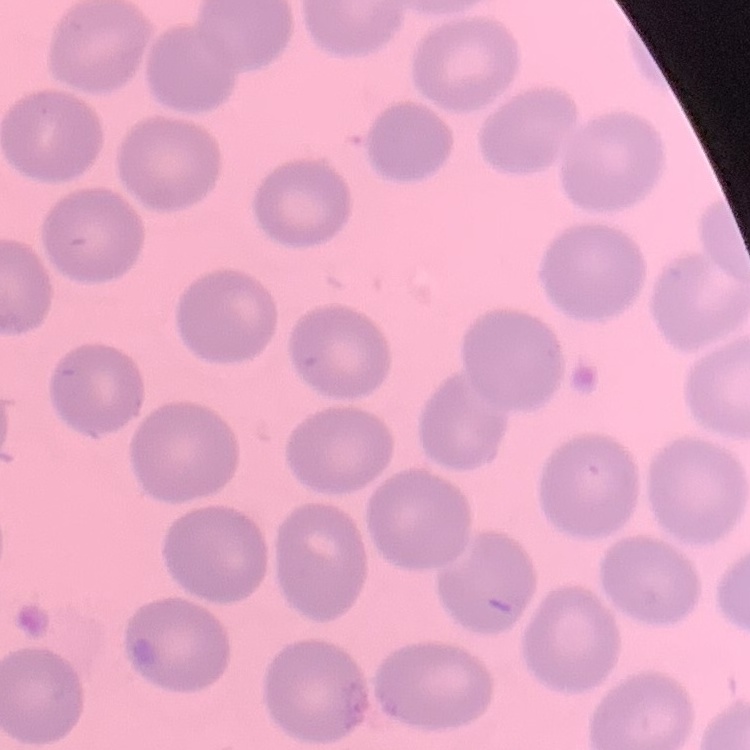
{
  "red_blood_cell_morphology": "no rouleaux formation",
  "preparation": "thin blood smear",
  "stain": "Field's or Giemsa",
  "image_type": "square crop of a larger photomicrograph"
}